Name the blood parasite species.
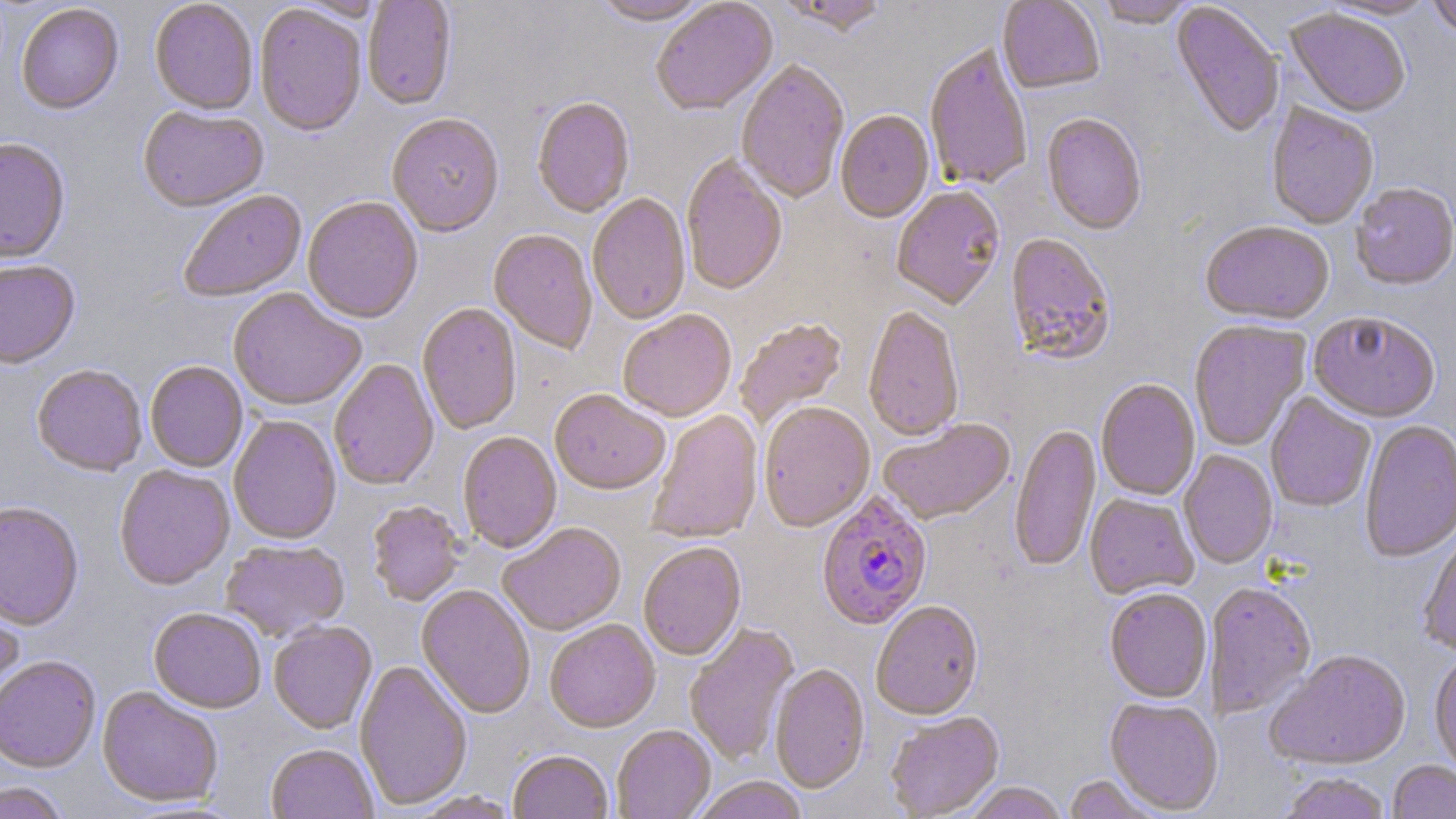

Plasmodium falciparum.

Approximate bounding boxes as named x1/y1/x2/y2 corners in pixels. Plasmodium falciparum-infected red blood cell locations: (x1=817, y1=494, x2=932, y2=632). Uninfected red blood cell locations: (x1=363, y1=0, x2=456, y2=112), (x1=776, y1=0, x2=891, y2=38), (x1=997, y1=0, x2=1105, y2=97), (x1=1321, y1=0, x2=1439, y2=21), (x1=1426, y1=0, x2=1456, y2=41), (x1=149, y1=1, x2=258, y2=117), (x1=592, y1=1, x2=712, y2=28), (x1=651, y1=1, x2=778, y2=118), (x1=1095, y1=1, x2=1199, y2=30), (x1=1170, y1=3, x2=1284, y2=139), (x1=16, y1=5, x2=124, y2=117), (x1=255, y1=6, x2=367, y2=139), (x1=1285, y1=10, x2=1410, y2=120), (x1=925, y1=46, x2=1032, y2=193), (x1=735, y1=61, x2=850, y2=205), (x1=532, y1=98, x2=635, y2=219), (x1=1266, y1=104, x2=1379, y2=230), (x1=138, y1=108, x2=268, y2=215), (x1=835, y1=112, x2=935, y2=225), (x1=1042, y1=114, x2=1146, y2=236), (x1=387, y1=115, x2=504, y2=239), (x1=0, y1=140, x2=70, y2=267), (x1=681, y1=156, x2=787, y2=298), (x1=1350, y1=184, x2=1456, y2=292), (x1=892, y1=187, x2=1006, y2=312), (x1=179, y1=191, x2=307, y2=303), (x1=587, y1=194, x2=691, y2=326), (x1=302, y1=199, x2=423, y2=325), (x1=1200, y1=223, x2=1335, y2=327), (x1=488, y1=230, x2=597, y2=355), (x1=1005, y1=234, x2=1115, y2=366), (x1=0, y1=262, x2=80, y2=371), (x1=228, y1=289, x2=365, y2=411), (x1=417, y1=303, x2=521, y2=436), (x1=863, y1=308, x2=964, y2=443), (x1=618, y1=311, x2=737, y2=423), (x1=1308, y1=314, x2=1440, y2=425), (x1=734, y1=319, x2=848, y2=430), (x1=1189, y1=321, x2=1310, y2=452), (x1=329, y1=360, x2=439, y2=492), (x1=145, y1=362, x2=248, y2=473), (x1=31, y1=366, x2=147, y2=478), (x1=1096, y1=379, x2=1200, y2=501), (x1=550, y1=391, x2=669, y2=496), (x1=1265, y1=394, x2=1376, y2=513), (x1=759, y1=404, x2=875, y2=533), (x1=647, y1=410, x2=763, y2=545), (x1=228, y1=416, x2=341, y2=546), (x1=879, y1=420, x2=1016, y2=527), (x1=1360, y1=420, x2=1456, y2=564), (x1=1009, y1=424, x2=1101, y2=573), (x1=458, y1=433, x2=562, y2=554), (x1=1178, y1=451, x2=1278, y2=570), (x1=114, y1=466, x2=235, y2=592), (x1=1084, y1=495, x2=1199, y2=600), (x1=367, y1=502, x2=464, y2=607), (x1=0, y1=503, x2=84, y2=633), (x1=498, y1=524, x2=627, y2=637), (x1=1418, y1=525, x2=1456, y2=658), (x1=221, y1=541, x2=350, y2=643), (x1=639, y1=544, x2=746, y2=662), (x1=1206, y1=583, x2=1316, y2=719), (x1=416, y1=586, x2=535, y2=719), (x1=0, y1=589, x2=24, y2=716), (x1=1104, y1=590, x2=1212, y2=704), (x1=871, y1=602, x2=984, y2=723), (x1=149, y1=609, x2=266, y2=714), (x1=545, y1=620, x2=660, y2=734), (x1=268, y1=623, x2=377, y2=735), (x1=684, y1=624, x2=799, y2=766), (x1=1264, y1=652, x2=1412, y2=771), (x1=1429, y1=654, x2=1456, y2=777), (x1=0, y1=657, x2=101, y2=774), (x1=354, y1=661, x2=472, y2=810), (x1=770, y1=664, x2=870, y2=794), (x1=97, y1=688, x2=223, y2=809), (x1=1104, y1=698, x2=1223, y2=815), (x1=885, y1=713, x2=1004, y2=819), (x1=612, y1=726, x2=716, y2=819), (x1=266, y1=744, x2=378, y2=819), (x1=508, y1=751, x2=614, y2=819), (x1=1388, y1=762, x2=1456, y2=819), (x1=1278, y1=773, x2=1391, y2=819), (x1=1062, y1=774, x2=1166, y2=818), (x1=692, y1=777, x2=808, y2=819), (x1=0, y1=782, x2=69, y2=818), (x1=965, y1=783, x2=1068, y2=819), (x1=410, y1=792, x2=521, y2=819). Thin blood smear. 1000x magnification. One field of a larger specimen. Light microscopy. May-Grünwald-Giemsa stain. Image is 1456×819 pixels.